State which parasite is depicted.
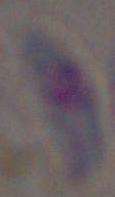

This is Toxoplasma gondii.

modality: photomicrograph
magnification: 1000x